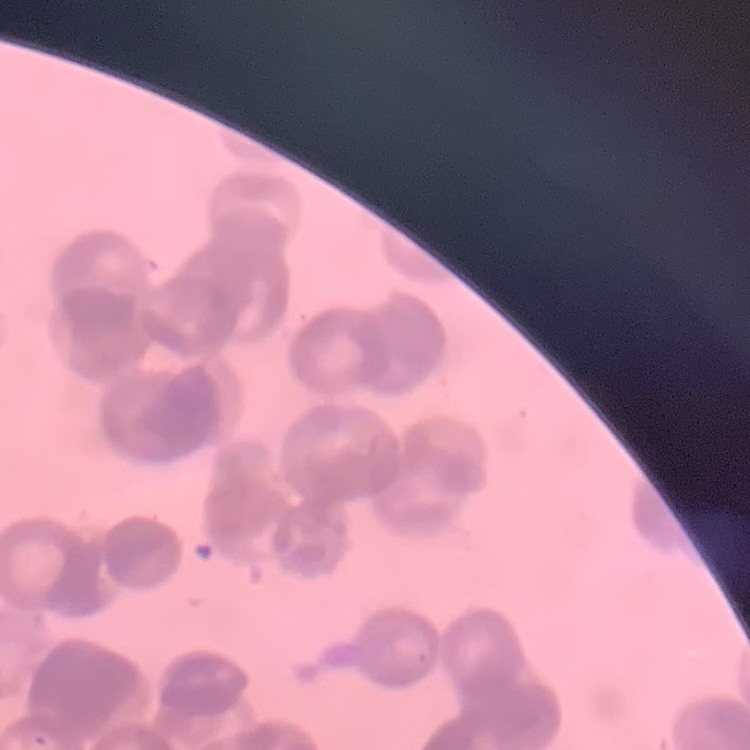
Summary:
  - Red blood cell morphology: rouleaux formation
  - Stain: Field's or Giemsa
  - Preparation: thin blood smear
  - Image type: one tile cut from a larger photomicrograph